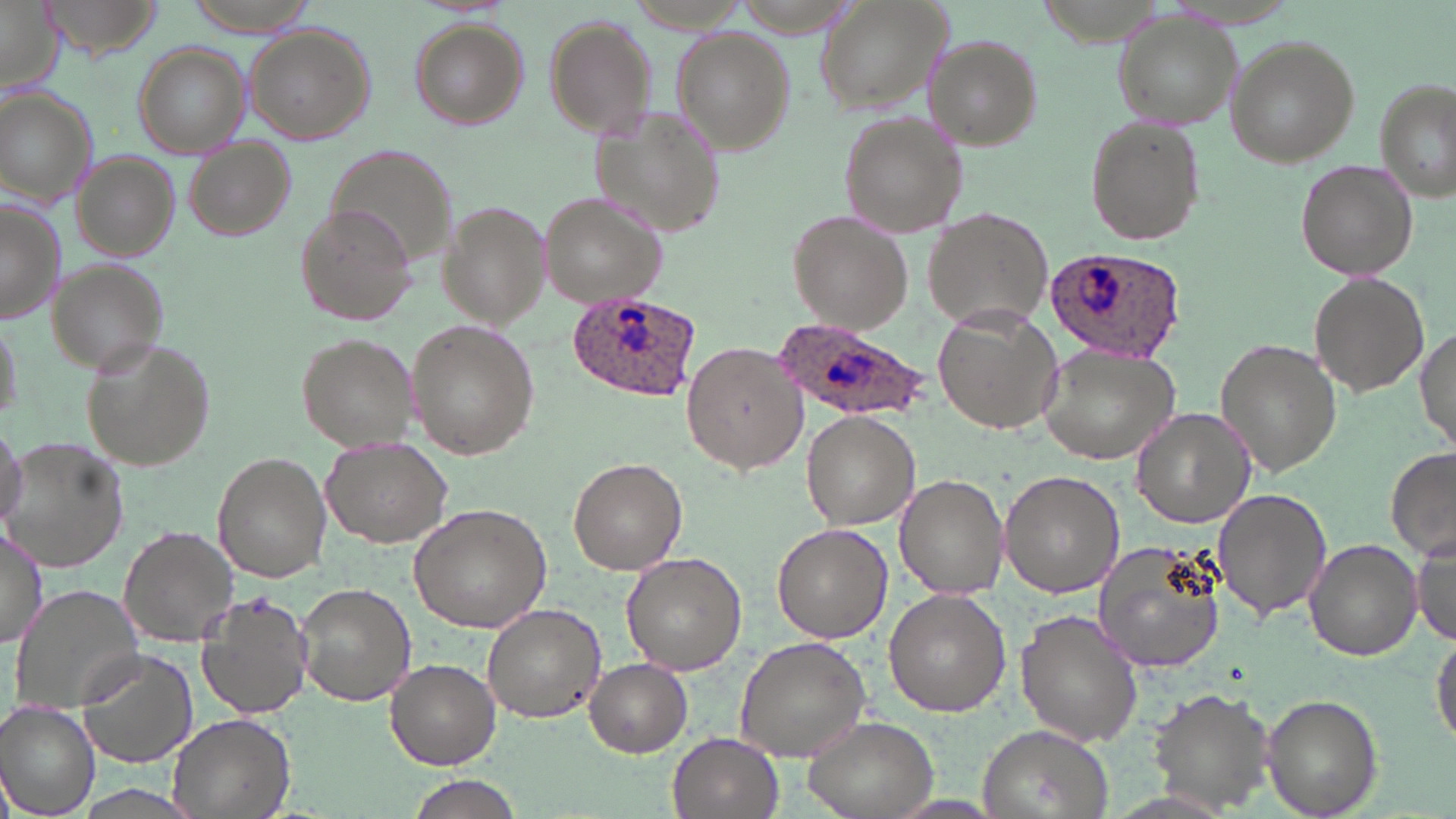
Plasmodium ovale-infected red blood cell locations = approximate bounding boxes as [x1, y1, x2, y2] in pixels: [1044, 247, 1190, 364], [564, 291, 703, 403], [773, 315, 930, 422]
slide-level diagnosis = Plasmodium ovale
image size = 1456×819 pixels
uninfected red blood cell locations = approximate bounding boxes as [x1, y1, x2, y2] in pixels: [38, 0, 165, 59], [181, 0, 323, 34], [813, 0, 951, 115], [0, 1, 63, 97], [543, 13, 658, 140], [1110, 14, 1241, 132], [409, 19, 526, 128], [243, 24, 375, 146], [673, 28, 796, 155], [1222, 34, 1360, 166], [923, 36, 1044, 149], [131, 43, 250, 157], [1374, 78, 1455, 203], [0, 87, 96, 205], [591, 104, 722, 241], [837, 112, 966, 239], [1083, 114, 1205, 248], [183, 142, 294, 243], [326, 145, 458, 274], [73, 150, 181, 261], [1295, 158, 1418, 282], [543, 191, 670, 309], [0, 202, 63, 323], [436, 202, 548, 328], [295, 203, 421, 326], [923, 208, 1054, 328], [787, 210, 912, 334], [46, 258, 168, 375], [1310, 273, 1428, 396], [933, 307, 1063, 436], [0, 308, 20, 428], [405, 318, 542, 461], [1414, 324, 1455, 451], [295, 333, 416, 453], [82, 336, 216, 474], [1216, 338, 1341, 476], [682, 341, 806, 474], [1035, 343, 1182, 465], [1130, 407, 1254, 530], [801, 411, 920, 530], [0, 416, 28, 530], [1, 437, 133, 573], [323, 440, 451, 547], [1386, 447, 1456, 563], [213, 454, 331, 582], [568, 457, 687, 574], [1000, 468, 1126, 597], [894, 473, 1010, 597], [1213, 489, 1332, 620], [410, 502, 553, 632], [773, 521, 892, 643], [0, 523, 48, 650], [118, 526, 237, 643], [1411, 529, 1456, 647], [1093, 537, 1225, 674], [1304, 539, 1424, 661], [620, 553, 750, 676], [296, 583, 415, 705], [13, 585, 148, 714], [884, 591, 1011, 717], [197, 594, 315, 721], [481, 602, 606, 722], [1014, 609, 1143, 747], [1432, 624, 1456, 753], [734, 636, 871, 763], [75, 650, 197, 769], [385, 659, 502, 769], [586, 659, 692, 757], [1150, 689, 1275, 811], [1261, 693, 1385, 818], [0, 703, 100, 817], [168, 712, 295, 819], [799, 714, 939, 819], [975, 724, 1113, 819], [668, 732, 786, 819], [405, 779, 522, 819]
modality = light microscopy
preparation = thin blood smear
magnification = 1000x
field of view = single
stain = May-Grünwald-Giemsa